Identify the blood parasite species.
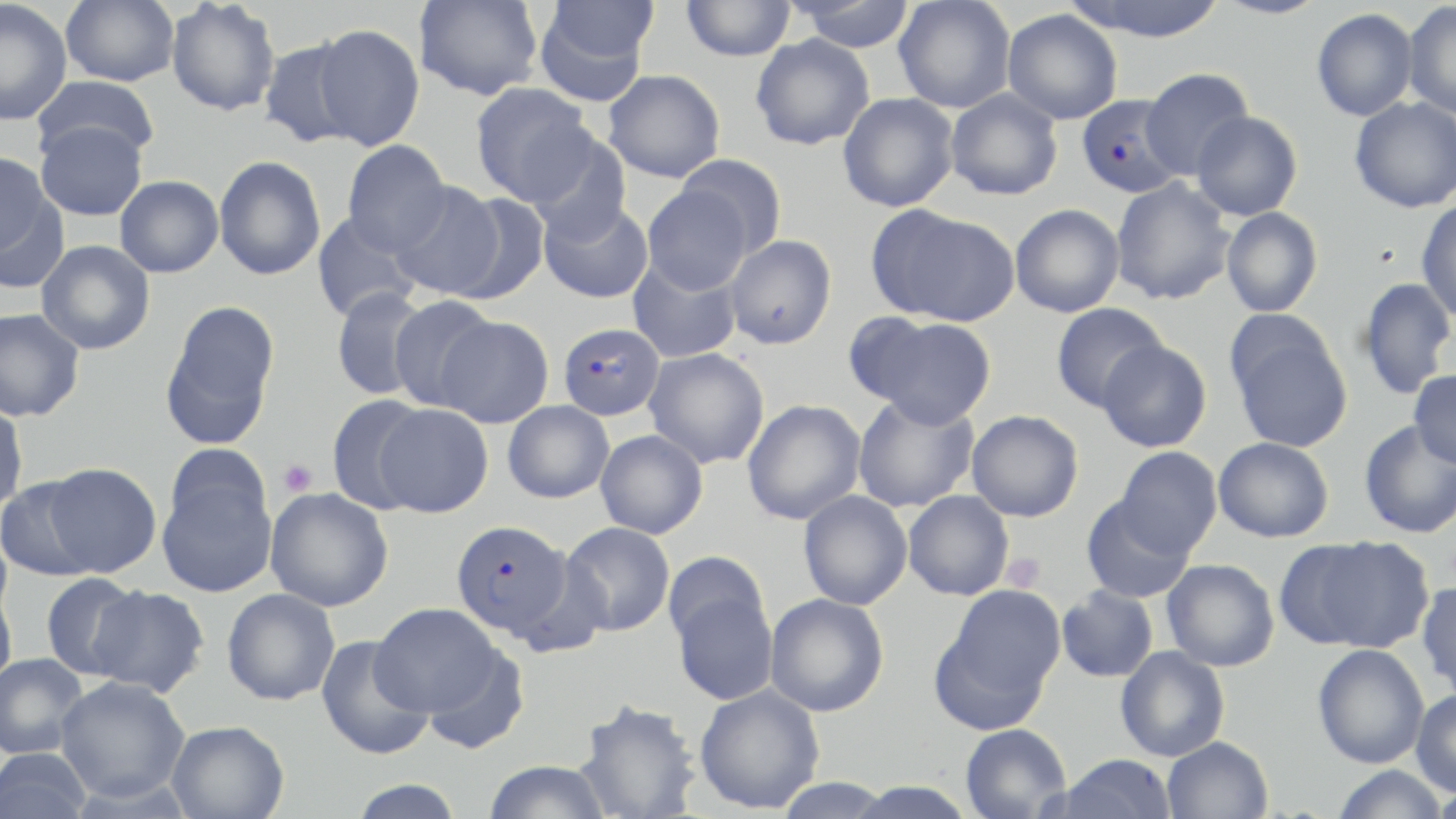
Plasmodium falciparum.

Approximate bounding boxes as named x1/y1/x2/y2 corners in pixels. Platelet locations: (x1=279, y1=459, x2=317, y2=496), (x1=1002, y1=552, x2=1046, y2=591). Plasmodium falciparum-infected red blood cell locations: (x1=1075, y1=94, x2=1183, y2=199), (x1=557, y1=322, x2=665, y2=422), (x1=450, y1=519, x2=571, y2=639). Uninfected red blood cell locations: (x1=61, y1=0, x2=180, y2=86), (x1=415, y1=0, x2=543, y2=100), (x1=681, y1=0, x2=795, y2=61), (x1=786, y1=0, x2=917, y2=52), (x1=894, y1=0, x2=1016, y2=113), (x1=1065, y1=0, x2=1229, y2=42), (x1=1212, y1=0, x2=1330, y2=20), (x1=1402, y1=0, x2=1456, y2=119), (x1=0, y1=1, x2=72, y2=126), (x1=166, y1=1, x2=280, y2=116), (x1=534, y1=1, x2=655, y2=105), (x1=1311, y1=8, x2=1418, y2=121), (x1=1002, y1=9, x2=1123, y2=124), (x1=312, y1=23, x2=425, y2=151), (x1=750, y1=33, x2=875, y2=150), (x1=259, y1=38, x2=361, y2=149), (x1=1141, y1=68, x2=1253, y2=179), (x1=603, y1=70, x2=725, y2=182), (x1=31, y1=75, x2=160, y2=164), (x1=470, y1=82, x2=596, y2=206), (x1=946, y1=88, x2=1063, y2=200), (x1=838, y1=92, x2=959, y2=212), (x1=1350, y1=96, x2=1456, y2=213), (x1=1191, y1=111, x2=1303, y2=221), (x1=35, y1=121, x2=147, y2=221), (x1=524, y1=129, x2=632, y2=242), (x1=342, y1=140, x2=452, y2=254), (x1=0, y1=152, x2=58, y2=269), (x1=676, y1=153, x2=788, y2=259), (x1=214, y1=155, x2=326, y2=280), (x1=115, y1=175, x2=223, y2=278), (x1=1111, y1=178, x2=1236, y2=305), (x1=391, y1=181, x2=506, y2=300), (x1=642, y1=185, x2=750, y2=294), (x1=446, y1=192, x2=550, y2=304), (x1=1416, y1=197, x2=1456, y2=323), (x1=539, y1=198, x2=653, y2=303), (x1=1010, y1=203, x2=1125, y2=317), (x1=870, y1=206, x2=1018, y2=327), (x1=1221, y1=207, x2=1323, y2=318), (x1=311, y1=213, x2=421, y2=322), (x1=725, y1=235, x2=837, y2=349), (x1=36, y1=240, x2=155, y2=355), (x1=628, y1=256, x2=742, y2=363), (x1=1357, y1=277, x2=1456, y2=401), (x1=331, y1=287, x2=432, y2=400), (x1=388, y1=297, x2=500, y2=412), (x1=159, y1=300, x2=280, y2=449), (x1=1050, y1=303, x2=1168, y2=412), (x1=0, y1=308, x2=85, y2=422), (x1=853, y1=313, x2=997, y2=428), (x1=435, y1=315, x2=554, y2=428), (x1=1227, y1=317, x2=1353, y2=454), (x1=1097, y1=339, x2=1212, y2=453), (x1=644, y1=348, x2=769, y2=468), (x1=1410, y1=369, x2=1456, y2=469), (x1=852, y1=393, x2=979, y2=513), (x1=325, y1=394, x2=431, y2=513), (x1=742, y1=399, x2=866, y2=525), (x1=0, y1=401, x2=28, y2=516), (x1=502, y1=401, x2=614, y2=503), (x1=374, y1=402, x2=493, y2=517), (x1=966, y1=410, x2=1084, y2=522), (x1=1359, y1=420, x2=1456, y2=539), (x1=595, y1=430, x2=708, y2=538), (x1=1213, y1=437, x2=1334, y2=543), (x1=1114, y1=446, x2=1222, y2=557), (x1=43, y1=462, x2=162, y2=578), (x1=157, y1=464, x2=277, y2=598), (x1=0, y1=476, x2=100, y2=582), (x1=266, y1=487, x2=394, y2=611), (x1=798, y1=490, x2=912, y2=610), (x1=903, y1=491, x2=1014, y2=600), (x1=1080, y1=495, x2=1196, y2=603), (x1=560, y1=522, x2=675, y2=636), (x1=1285, y1=536, x2=1434, y2=653), (x1=662, y1=550, x2=770, y2=653), (x1=1162, y1=559, x2=1279, y2=672), (x1=40, y1=572, x2=145, y2=680), (x1=668, y1=577, x2=778, y2=707), (x1=1417, y1=580, x2=1456, y2=700), (x1=930, y1=584, x2=1065, y2=732), (x1=0, y1=586, x2=17, y2=691), (x1=89, y1=586, x2=211, y2=698), (x1=1057, y1=587, x2=1159, y2=683), (x1=221, y1=588, x2=340, y2=706), (x1=765, y1=593, x2=889, y2=716), (x1=370, y1=603, x2=502, y2=718), (x1=316, y1=634, x2=435, y2=761), (x1=421, y1=644, x2=531, y2=755), (x1=1313, y1=644, x2=1430, y2=769), (x1=1115, y1=646, x2=1230, y2=762), (x1=0, y1=653, x2=90, y2=759), (x1=56, y1=677, x2=191, y2=800), (x1=694, y1=684, x2=825, y2=814), (x1=1411, y1=690, x2=1456, y2=796), (x1=574, y1=699, x2=701, y2=819), (x1=165, y1=720, x2=289, y2=819), (x1=960, y1=723, x2=1072, y2=818), (x1=1162, y1=736, x2=1273, y2=819), (x1=0, y1=747, x2=94, y2=819), (x1=1056, y1=754, x2=1176, y2=818), (x1=483, y1=760, x2=612, y2=819), (x1=1330, y1=765, x2=1449, y2=818), (x1=346, y1=779, x2=467, y2=818), (x1=1428, y1=782, x2=1456, y2=818). Image is 1456×819 pixels. Thin blood smear. Light microscopy. May-Grünwald-Giemsa stain. Captured at 1000x magnification. One field of a larger specimen.